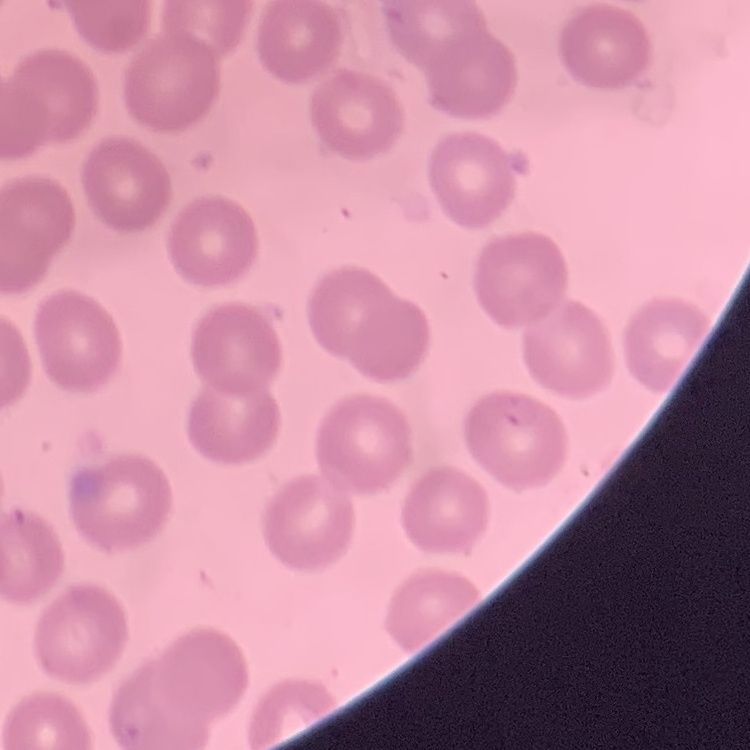
Summary:
  - Red blood cell morphology: no rouleaux formation
  - Image type: one tile cut from a larger photomicrograph
  - Stain: Field's or Giemsa
  - Preparation: thin blood smear